Classify this cell by malaria status.
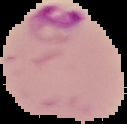

It is parasitized.

image size = 127×124 pixels
preparation = thin blood film
image type = segmented cell region on a black background